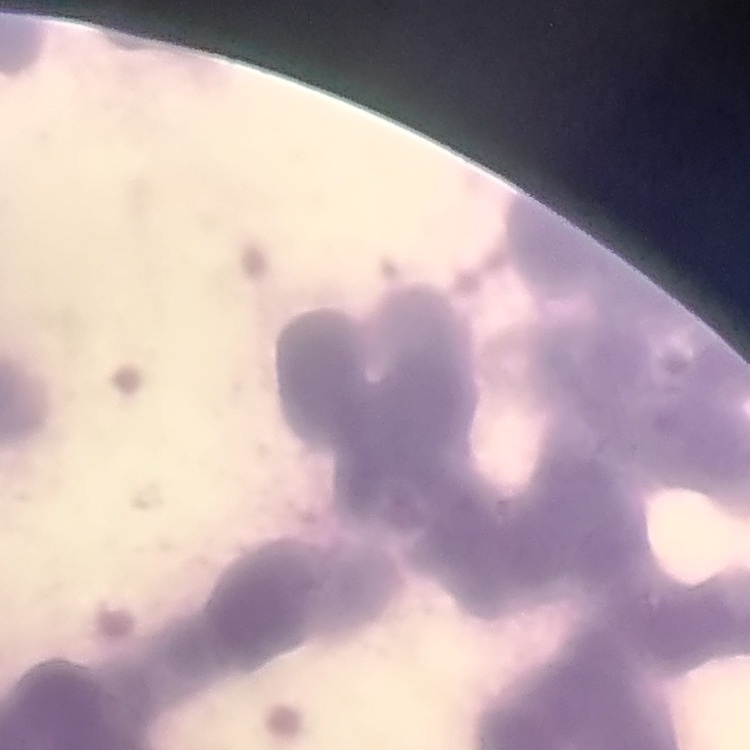

erythrocyte morphology = rouleaux formation
preparation = thin blood film
stain = Field's or Giemsa
image type = square crop of a larger photomicrograph